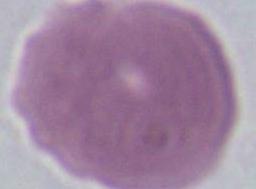
Summary:
  - Identification: erythrocyte
  - Modality: photomicrograph
  - Magnification: 1000x